Describe the morphology of the erythrocytes.
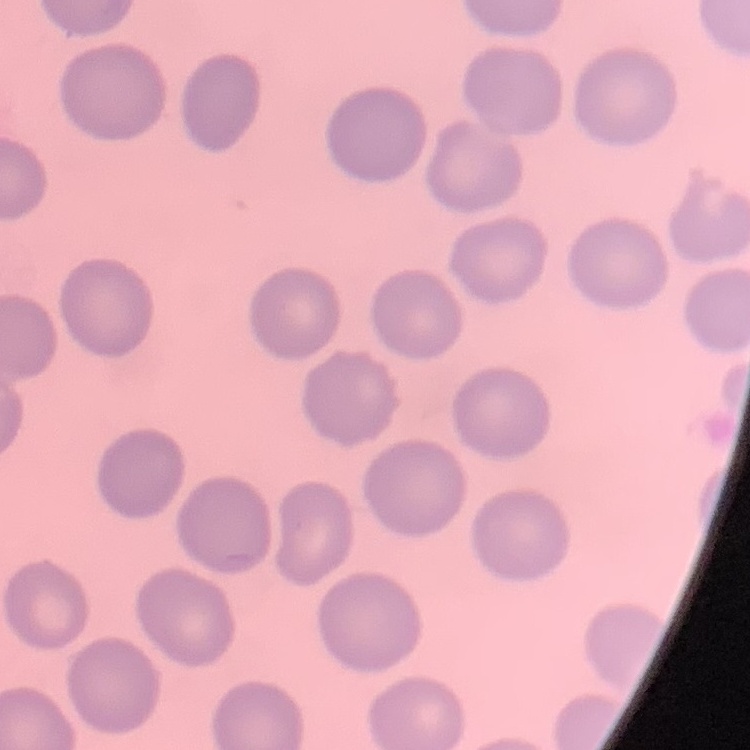
They show no rouleaux formation.

Summary:
  - Image type: square crop of a larger photomicrograph
  - Stain: Field's or Giemsa
  - Preparation: thin peripheral smear